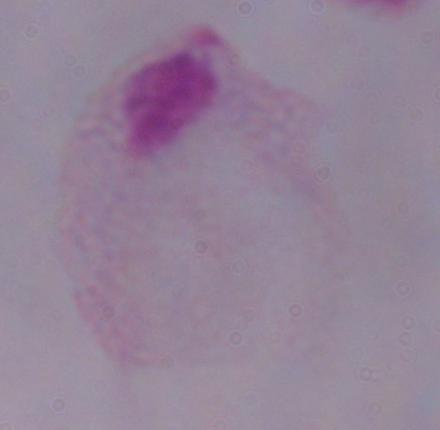
modality: photomicrograph
magnification: 1000x
identification: trichomonad